Report the malaria status of this cell.
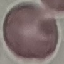

Uninfected.

Thin blood film. Cell patch, automatically extracted from a larger field of view and resized to 64 × 64 pixels. Photographed with a smartphone camera at the microscope eyepiece. Giemsa-stained preparation.